Identify the cell.
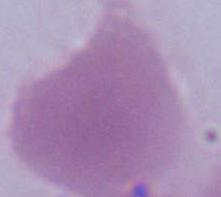
An erythrocyte.

{
  "modality": "micrograph",
  "magnification": "1000x"
}